Identify the blood parasite species.
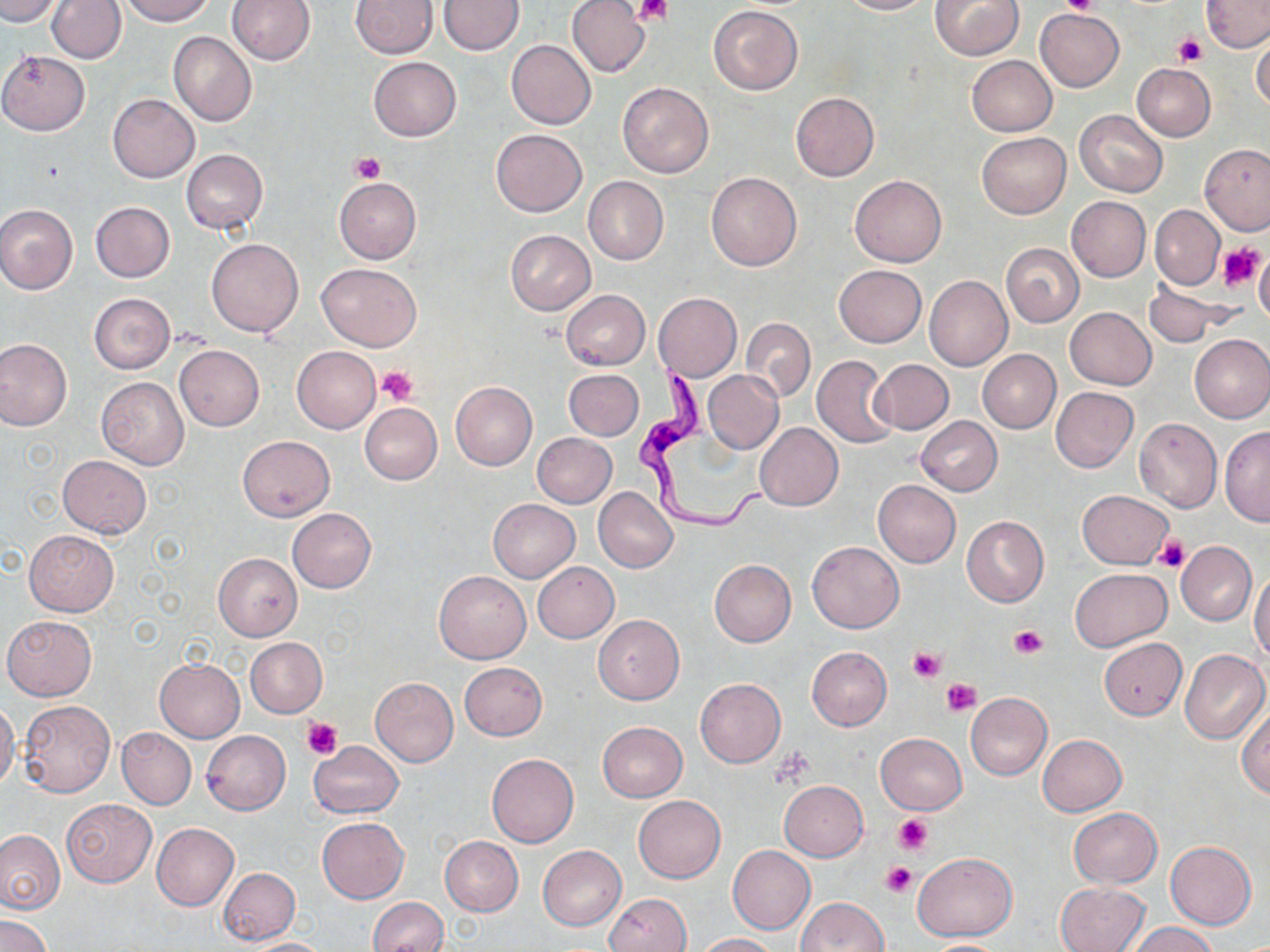

Trypanosoma brucei.

preparation = thin blood film
uninfected red blood cell locations = approximate bounding boxes as (x1,y1)-(x2,y2) corner pairs in pixels: (0,0)-(61,25), (47,0)-(126,64), (120,0)-(216,25), (228,0)-(315,64), (350,0)-(437,58), (441,0)-(522,54), (567,0)-(650,77), (838,0)-(932,15), (932,0)-(1023,59), (1202,0)-(1269,52), (709,6)-(803,95), (1036,9)-(1123,91), (168,31)-(256,127), (1251,34)-(1270,112), (507,39)-(596,129), (0,51)-(90,135), (967,55)-(1057,137), (369,57)-(460,141), (1132,63)-(1215,142), (617,81)-(714,178), (791,91)-(879,181), (108,94)-(199,182), (1074,109)-(1167,197), (491,129)-(586,215), (976,133)-(1071,219), (1200,145)-(1270,235), (181,149)-(266,235), (706,172)-(802,272), (583,175)-(668,264), (849,175)-(947,267), (335,177)-(421,263), (1067,196)-(1150,281), (91,202)-(175,282), (0,205)-(78,294), (1149,206)-(1224,290), (505,230)-(596,314), (206,238)-(303,337), (1001,243)-(1085,327), (1255,250)-(1269,327), (316,262)-(423,351), (834,265)-(926,347), (924,274)-(1014,370), (1143,282)-(1239,347), (561,290)-(650,369), (89,293)-(175,374), (653,293)-(741,381), (1064,308)-(1156,390), (740,318)-(815,403), (1189,334)-(1270,423), (0,338)-(72,430), (174,344)-(264,431), (292,346)-(381,433), (978,350)-(1061,433), (812,354)-(898,448), (870,359)-(953,434), (564,369)-(644,440), (703,371)-(784,453), (97,377)-(189,470), (451,382)-(537,469), (1050,387)-(1138,472), (360,402)-(442,484), (916,416)-(1002,496), (1133,417)-(1222,512), (756,423)-(843,511), (1219,425)-(1270,527), (532,433)-(617,508), (238,436)-(334,520), (57,454)-(151,538), (873,479)-(961,567), (595,488)-(678,572), (1076,489)-(1174,569), (488,499)-(580,581), (287,509)-(376,593), (962,516)-(1048,607), (23,530)-(119,616), (807,541)-(904,633), (1176,541)-(1256,626), (213,553)-(302,641), (709,559)-(796,646), (534,562)-(618,643), (1070,567)-(1171,651), (1249,569)-(1270,662), (434,570)-(531,664), (593,615)-(684,704), (3,616)-(96,700), (245,638)-(327,717), (1099,638)-(1186,720), (807,646)-(891,730), (1180,650)-(1270,745), (154,658)-(245,741), (459,662)-(548,740), (370,678)-(459,766), (695,678)-(785,767), (965,692)-(1052,780), (18,700)-(115,797), (0,701)-(20,793), (1237,702)-(1270,797), (597,721)-(688,801), (116,727)-(195,809), (201,730)-(289,815), (876,733)-(966,814), (1038,734)-(1127,815), (308,741)-(403,818), (487,753)-(580,847), (778,781)-(868,861), (633,795)-(726,883), (62,799)-(156,887), (1068,808)-(1162,888), (317,817)-(408,903), (151,823)-(238,911), (0,830)-(65,914), (439,836)-(523,916), (1165,841)-(1256,929), (537,846)-(626,930), (727,846)-(815,934), (913,850)-(1016,941), (218,868)-(300,944), (1055,882)-(1150,951), (605,892)-(692,952), (368,897)-(448,952), (794,897)-(889,951), (0,914)-(52,951), (1127,921)-(1220,952), (694,933)-(778,952), (237,937)-(333,951), (921,939)-(1012,951)
Trypanosoma brucei locations = approximate bounding boxes as (x1,y1)-(x2,y2) corner pairs in pixels: (633,357)-(772,533)
stain = May-Grünwald-Giemsa
field of view = single
platelet locations = approximate bounding boxes as (x1,y1)-(x2,y2) corner pairs in pixels: (635,0)-(671,26), (1062,0)-(1101,15), (1172,32)-(1206,66), (351,154)-(386,185), (1217,242)-(1267,291), (376,366)-(418,406), (1153,535)-(1189,572), (1008,625)-(1048,659), (909,645)-(944,683), (941,677)-(981,716), (301,718)-(341,758), (773,747)-(816,784), (894,815)-(933,854), (882,861)-(917,896)
image size = 1270×952 pixels
modality = optical microscopy
magnification = 1000x